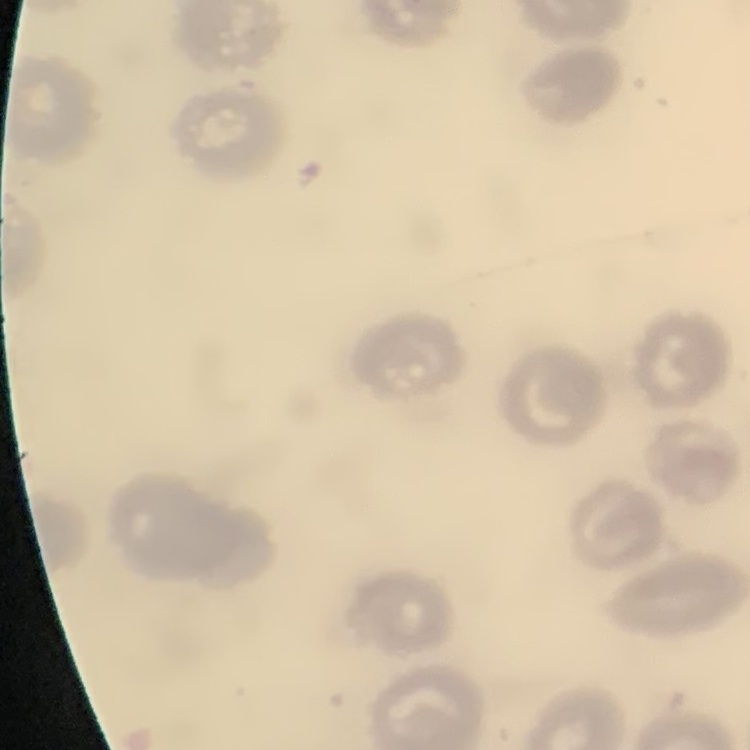

Summary:
  - Red blood cell morphology: no rouleaux formation
  - Image type: square crop of a larger photomicrograph
  - Preparation: thin blood smear
  - Stain: Field's or Giemsa